State the blood parasite species.
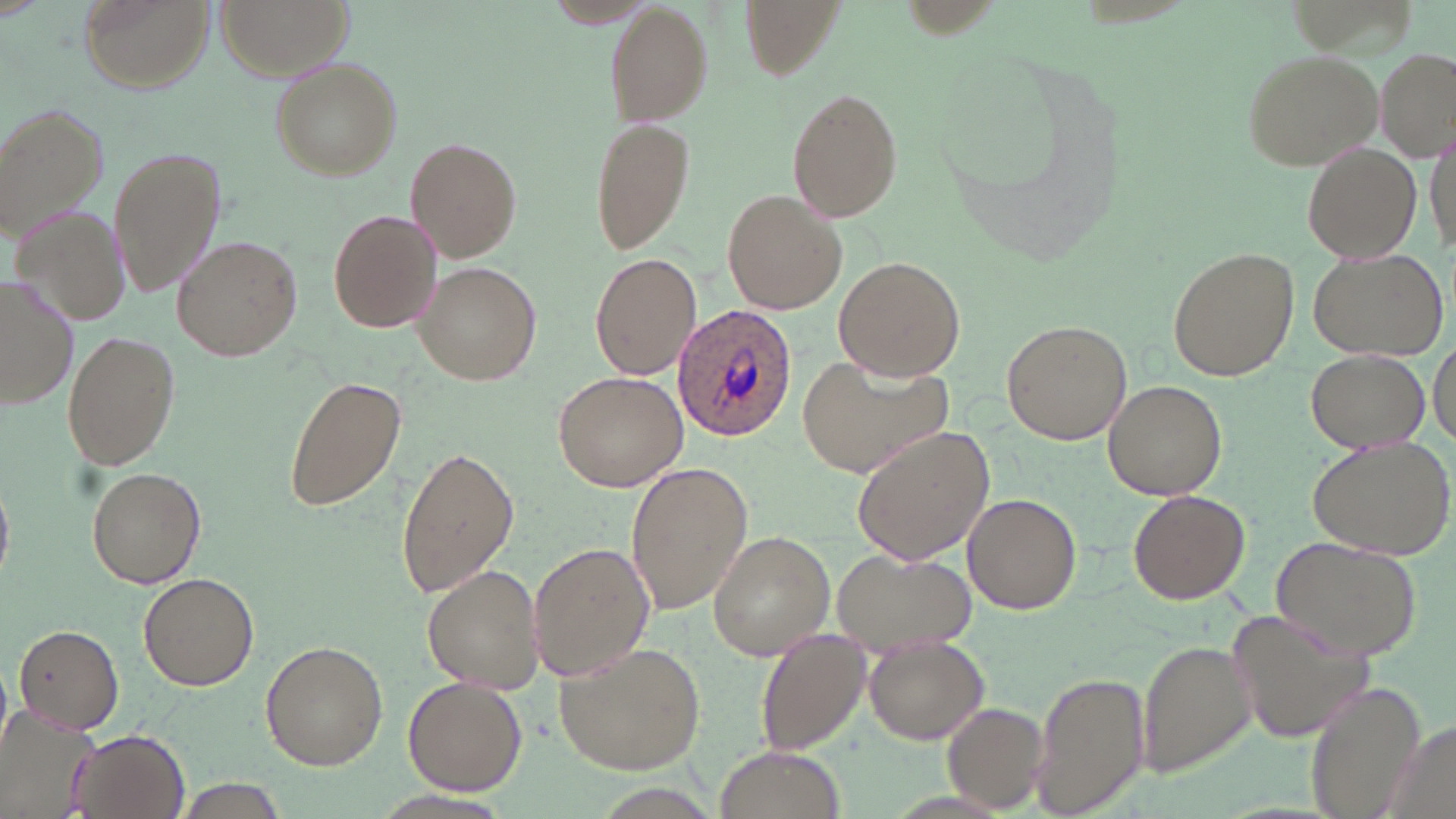
Plasmodium ovale.

Summary:
  - Coordinate format: approximate bounding boxes as (x1, y1, x2, y2) in pixels
  - Uninfected red blood cell locations: (78, 0, 217, 94), (216, 0, 350, 77), (735, 0, 847, 80), (539, 1, 662, 30), (603, 5, 712, 122), (1241, 48, 1386, 171), (1379, 49, 1455, 157), (268, 57, 402, 179), (786, 87, 903, 220), (0, 102, 110, 238), (591, 114, 695, 253), (406, 137, 522, 262), (1301, 142, 1421, 263), (110, 145, 225, 297), (722, 187, 848, 317), (11, 206, 133, 330), (329, 210, 441, 333), (173, 236, 300, 361), (1166, 248, 1298, 381), (1307, 249, 1447, 361), (590, 251, 702, 381), (834, 254, 964, 381), (414, 261, 541, 387), (1, 278, 78, 411), (1000, 318, 1132, 444), (62, 331, 179, 471), (1429, 338, 1454, 448), (1306, 350, 1430, 452), (554, 371, 688, 493), (283, 376, 405, 512), (1103, 379, 1226, 499), (850, 423, 994, 564), (1308, 438, 1456, 558), (397, 443, 519, 599), (625, 461, 753, 616), (88, 465, 206, 588), (0, 482, 14, 580), (1129, 488, 1250, 604), (961, 493, 1083, 614), (706, 530, 834, 659), (1267, 535, 1424, 663), (528, 539, 656, 684), (829, 546, 975, 656), (422, 564, 546, 694), (138, 572, 258, 690), (1226, 603, 1375, 746), (13, 623, 124, 734), (754, 631, 868, 752), (862, 637, 987, 745), (1139, 637, 1258, 777), (260, 640, 387, 770), (553, 641, 707, 774), (1031, 668, 1146, 818), (402, 675, 528, 795), (1307, 682, 1425, 815), (4, 699, 99, 817), (942, 702, 1047, 811), (66, 729, 191, 818), (716, 745, 841, 817), (175, 778, 289, 819)
  - Plasmodium ovale-infected red blood cell locations: (672, 303, 798, 442)
  - Stain: May-Grünwald-Giemsa
  - Modality: optical microscopy
  - Magnification: 1000x
  - Preparation: thin blood smear
  - Image size: 1456×819 pixels
  - Field of view: single